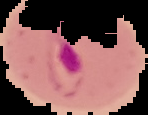 Image is 148×115 pixels. Malaria status: parasitized. From a thin blood film. The area outside the segmented cell region is set to black.